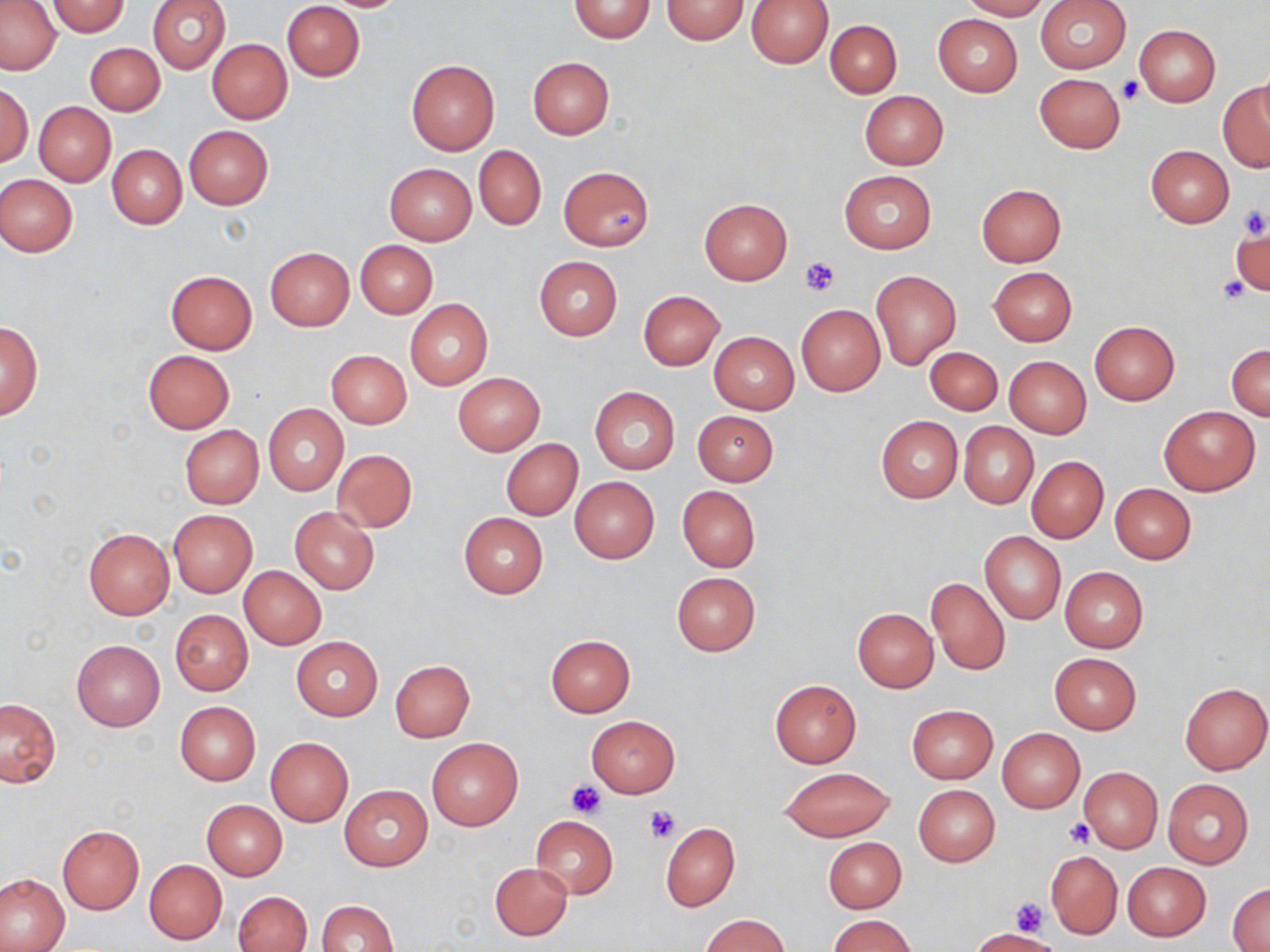
Approximate bounding boxes as [x1, y1, x2, y2] in pixels. Uninfected red blood cell locations: [147, 0, 230, 73], [568, 0, 656, 43], [661, 0, 749, 45], [746, 0, 833, 69], [959, 0, 1051, 19], [44, 1, 131, 37], [281, 1, 365, 81], [1036, 1, 1130, 73], [0, 2, 61, 75], [106, 12, 221, 89], [932, 13, 1024, 96], [824, 19, 901, 97], [1134, 25, 1220, 107], [208, 39, 292, 123], [86, 43, 165, 115], [527, 57, 614, 140], [406, 60, 500, 156], [1034, 74, 1124, 153], [1218, 79, 1270, 173], [0, 83, 32, 167], [859, 90, 948, 169], [34, 102, 115, 186], [183, 125, 273, 209], [107, 144, 187, 229], [1145, 145, 1234, 227], [474, 146, 545, 230], [385, 163, 476, 245], [558, 166, 653, 251], [839, 170, 936, 253], [0, 174, 77, 257], [975, 183, 1066, 268], [699, 198, 792, 284], [1230, 224, 1270, 298], [355, 240, 437, 318], [265, 247, 354, 330], [533, 256, 622, 341], [988, 266, 1077, 346], [164, 270, 257, 355], [871, 270, 962, 368], [638, 290, 726, 370], [404, 299, 492, 390], [796, 304, 885, 395], [0, 320, 42, 420], [1090, 321, 1179, 404], [709, 331, 798, 414], [1226, 343, 1270, 419], [926, 346, 1002, 414], [143, 350, 234, 433], [326, 350, 411, 428], [1005, 356, 1091, 438], [452, 373, 545, 454], [590, 387, 680, 474], [263, 403, 347, 496], [1159, 405, 1260, 495], [693, 410, 777, 485], [876, 416, 962, 502], [958, 421, 1038, 508], [178, 425, 264, 509], [501, 439, 582, 521], [332, 450, 417, 532], [1026, 456, 1108, 542], [569, 476, 660, 563], [1110, 483, 1197, 564], [677, 485, 760, 572], [289, 506, 379, 594], [168, 510, 256, 597], [459, 512, 548, 598], [83, 528, 174, 620], [979, 530, 1065, 625], [1059, 566, 1148, 652], [239, 567, 326, 649], [671, 571, 761, 656], [925, 575, 1009, 676], [852, 608, 938, 693], [170, 609, 252, 695], [545, 635, 635, 716], [291, 636, 382, 721], [71, 639, 165, 731], [1049, 653, 1141, 734], [390, 660, 475, 741], [768, 679, 861, 768], [1180, 683, 1270, 774], [0, 698, 61, 787], [176, 702, 260, 785], [908, 704, 997, 783], [585, 716, 679, 797], [997, 728, 1085, 812], [265, 737, 353, 827], [426, 737, 523, 831], [1078, 767, 1163, 854], [781, 768, 892, 842], [1163, 779, 1253, 868], [913, 784, 999, 867], [339, 785, 432, 872], [202, 799, 287, 880], [531, 816, 617, 898], [661, 822, 739, 911], [57, 824, 144, 913], [822, 837, 906, 913], [1045, 850, 1122, 938], [145, 860, 227, 944], [1123, 862, 1210, 941], [490, 863, 572, 940], [0, 874, 71, 951], [1228, 883, 1269, 951], [235, 891, 312, 952], [316, 900, 399, 952], [702, 913, 789, 951], [829, 914, 916, 952], [974, 929, 1060, 952]. Platelet locations: [1117, 75, 1145, 104], [1236, 202, 1269, 240], [606, 208, 639, 237], [801, 257, 840, 296], [1217, 275, 1252, 302], [567, 780, 607, 819], [646, 806, 679, 842], [1065, 819, 1094, 847], [1010, 897, 1049, 937]. Slide-level diagnosis: no evidence of blood parasites. Image is 1270×952 pixels. One field of a larger specimen. Captured at 1000x magnification. May-Grünwald-Giemsa stain. Light microscopy. Thin blood film.